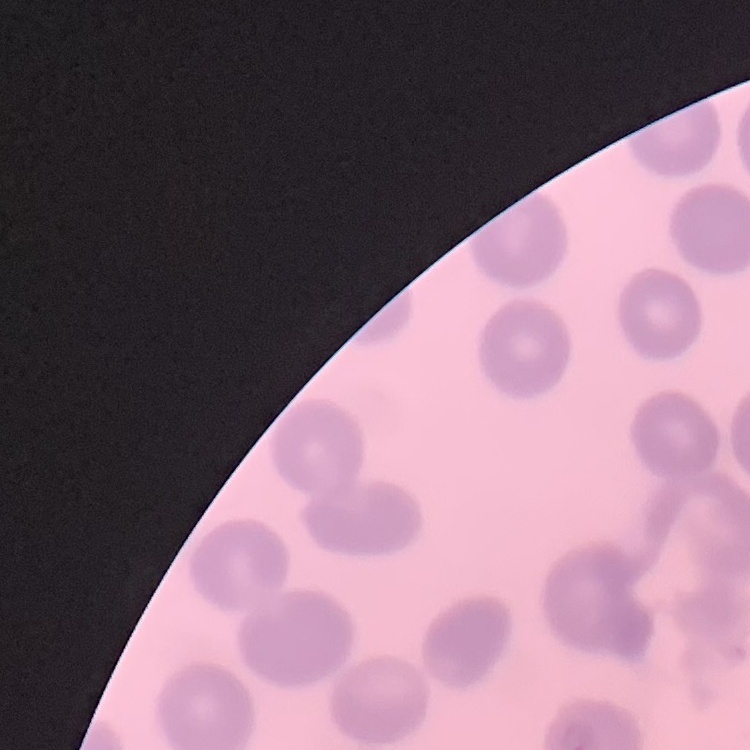
erythrocyte morphology = no rouleaux formation
preparation = thin blood smear
stain = Field's or Giemsa
image type = square crop of a larger photomicrograph